Locate every blood parasite and identify its species.
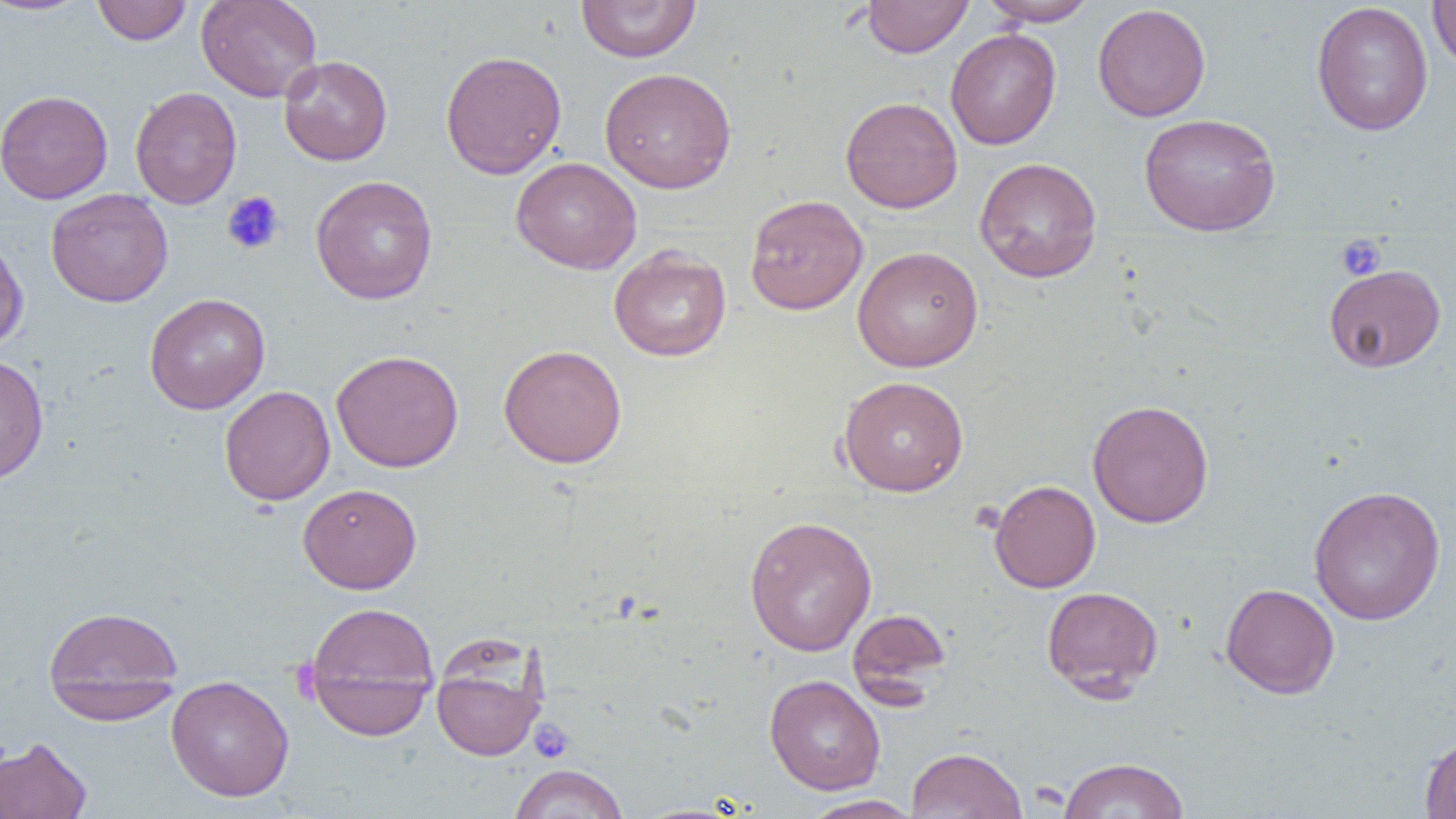
No blood parasites observed.

slide_level_diagnosis: no evidence of blood parasites
preparation: thin blood film
uninfected_red_blood_cell_locations: 'approximate bounding boxes as [x1, y1, x2, y2] in pixels: [0, 0, 92, 16], [195, 0, 323, 103], [576, 0, 701, 63], [861, 0, 972, 58], [979, 0, 1098, 27], [1428, 0, 1456, 71], [92, 1, 192, 45], [1311, 2, 1434, 136], [1092, 3, 1211, 122], [946, 29, 1061, 150], [440, 50, 567, 179], [279, 55, 393, 166], [599, 67, 737, 193], [130, 86, 242, 209], [0, 89, 113, 204], [840, 96, 962, 213], [1139, 112, 1280, 236], [974, 156, 1102, 283], [511, 157, 642, 274], [310, 175, 438, 305], [46, 188, 173, 307], [744, 194, 868, 315], [0, 231, 28, 353], [852, 245, 984, 372], [609, 246, 731, 362], [1324, 263, 1446, 372], [144, 293, 271, 414], [498, 343, 627, 468], [331, 349, 464, 472], [0, 354, 49, 487], [838, 375, 969, 496], [219, 385, 335, 505], [1087, 399, 1214, 528], [989, 480, 1101, 593], [298, 483, 422, 594], [1308, 485, 1446, 625], [744, 514, 877, 656], [1220, 583, 1340, 699], [1041, 585, 1164, 699], [304, 601, 440, 739], [43, 604, 184, 720], [846, 606, 951, 705], [430, 642, 547, 762], [765, 674, 886, 795], [166, 675, 294, 801], [1419, 732, 1456, 819], [0, 736, 92, 819], [906, 747, 1028, 819], [1058, 757, 1190, 819], [508, 763, 629, 818], [800, 795, 922, 818]'
field_of_view: single
image_size: 1456×819 pixels
modality: light microscopy
magnification: 1000x
platelet_locations: 'approximate bounding boxes as [x1, y1, x2, y2] in pixels: [222, 191, 285, 255], [1335, 235, 1387, 281], [529, 718, 575, 764]'